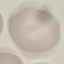

Malaria status: uninfected. Photographed with a smartphone camera at the microscope eyepiece. Cell patch, automatically extracted from a larger field of view and resized to 64 × 64 pixels. Giemsa stain. Thin blood smear.